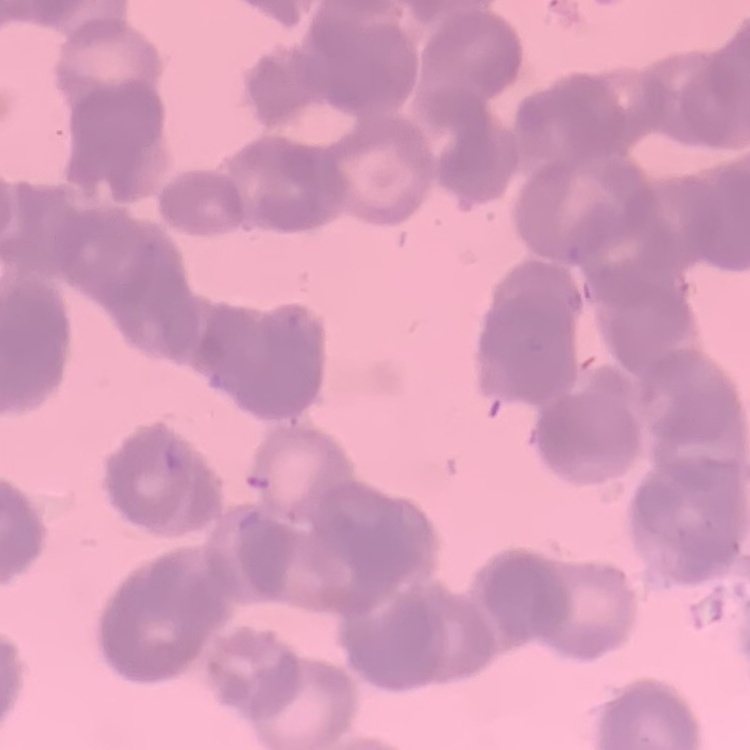

Summary:
  - Red blood cell morphology: rouleaux formation
  - Preparation: thin peripheral smear
  - Image type: one tile cut from a larger photomicrograph
  - Stain: Field's or Giemsa